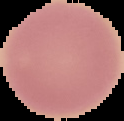
Image is 124×121 pixels. Result: no Plasmodium parasites detected. The area outside the segmented cell region is set to black. From a thin blood film.